Classify this cell by malaria status.
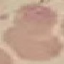

It is uninfected.

Acquired by smartphone through the microscope eyepiece. Thin blood film. Giemsa stain. Cell patch, automatically extracted from a larger field of view and resized to 64 × 64 pixels.